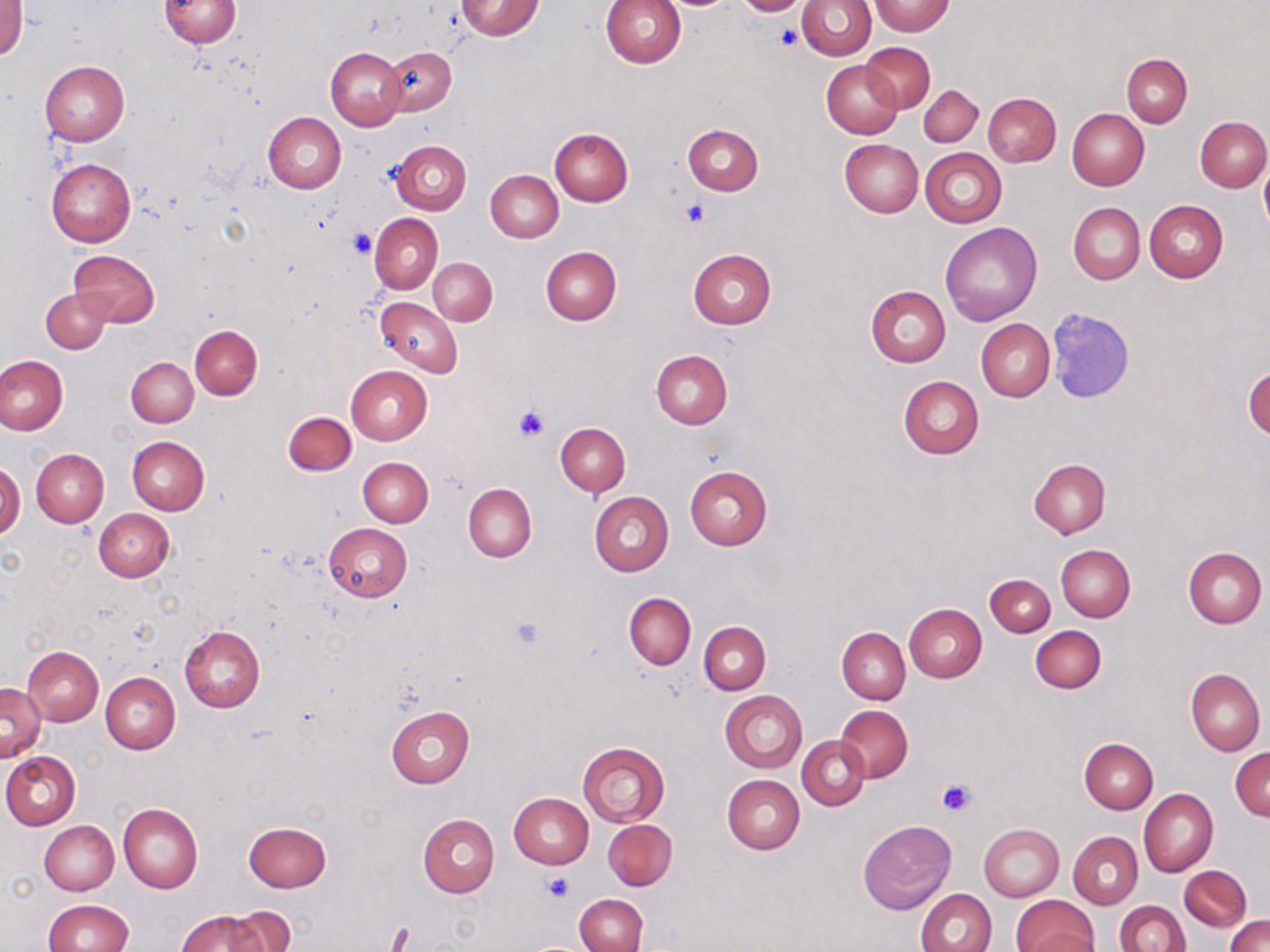
Approximate bounding boxes as (x1, y1, x2, y2) in pixels. Platelet locations: (773, 22, 802, 48), (681, 199, 710, 226), (349, 228, 375, 257), (514, 405, 549, 442), (508, 614, 546, 652), (936, 779, 977, 817), (543, 874, 574, 903), (384, 922, 416, 950). Uninfected red blood cell locations: (157, 0, 241, 49), (455, 0, 544, 40), (731, 0, 813, 16), (797, 0, 876, 60), (1, 1, 26, 62), (600, 1, 686, 70), (869, 1, 955, 36), (862, 43, 934, 112), (380, 46, 455, 117), (326, 47, 405, 131), (1122, 54, 1191, 126), (821, 59, 902, 139), (39, 61, 129, 146), (919, 85, 983, 147), (984, 93, 1060, 167), (1067, 109, 1148, 190), (264, 112, 346, 193), (1195, 117, 1270, 191), (683, 124, 763, 196), (550, 129, 633, 206), (839, 139, 923, 217), (393, 141, 471, 214), (920, 148, 1006, 227), (47, 158, 136, 247), (1259, 161, 1270, 237), (485, 169, 563, 243), (1144, 200, 1228, 282), (1069, 202, 1144, 284), (370, 212, 442, 293), (940, 223, 1042, 325), (541, 246, 621, 325), (688, 249, 775, 329), (70, 250, 159, 326), (428, 258, 498, 324), (866, 286, 951, 368), (41, 287, 112, 353), (375, 297, 462, 376), (1047, 306, 1134, 400), (975, 319, 1054, 402), (190, 324, 262, 399), (651, 349, 733, 429), (0, 355, 67, 435), (126, 357, 198, 427), (345, 365, 433, 444), (1243, 365, 1270, 442), (898, 375, 984, 460), (283, 411, 356, 476), (556, 422, 630, 496), (127, 436, 209, 515), (32, 448, 109, 527), (358, 456, 433, 527), (1028, 458, 1110, 538), (0, 462, 24, 540), (684, 466, 772, 550), (464, 483, 537, 562), (589, 491, 673, 576), (93, 508, 174, 581), (323, 523, 412, 602), (1056, 545, 1135, 622), (1183, 546, 1266, 628), (985, 574, 1055, 637), (624, 593, 696, 668), (904, 603, 987, 682), (699, 621, 771, 694), (179, 625, 266, 713), (1030, 625, 1106, 693), (837, 627, 910, 704), (23, 647, 103, 726), (1, 658, 82, 747), (1186, 668, 1265, 755), (100, 672, 180, 754), (1, 683, 46, 761), (720, 690, 806, 773), (385, 705, 475, 787), (837, 705, 912, 781), (798, 736, 869, 810), (1080, 738, 1158, 813), (577, 742, 670, 827), (1230, 747, 1270, 820), (2, 751, 80, 829), (723, 776, 805, 854), (1139, 788, 1218, 877), (509, 793, 593, 869), (119, 804, 203, 893), (418, 814, 499, 897), (603, 819, 676, 890), (40, 820, 119, 894), (858, 820, 956, 916), (244, 821, 331, 892), (978, 824, 1062, 900), (1069, 831, 1142, 909), (1180, 866, 1250, 931), (1129, 877, 1247, 938), (916, 888, 995, 952), (575, 894, 647, 952), (1010, 894, 1099, 952), (43, 900, 134, 952), (1114, 901, 1189, 952), (223, 906, 295, 952), (178, 910, 267, 952), (1225, 915, 1269, 952). Slide-level diagnosis: negative for blood parasites. One field of a larger specimen. Thin blood film. May-Grünwald-Giemsa stain. Captured at 1000x magnification. Light microscopy. Image is 1270×952 pixels.